Name the parasite shown.
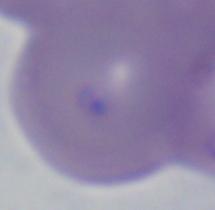

This is Babesia.

Summary:
  - Modality: micrograph
  - Magnification: 1000x